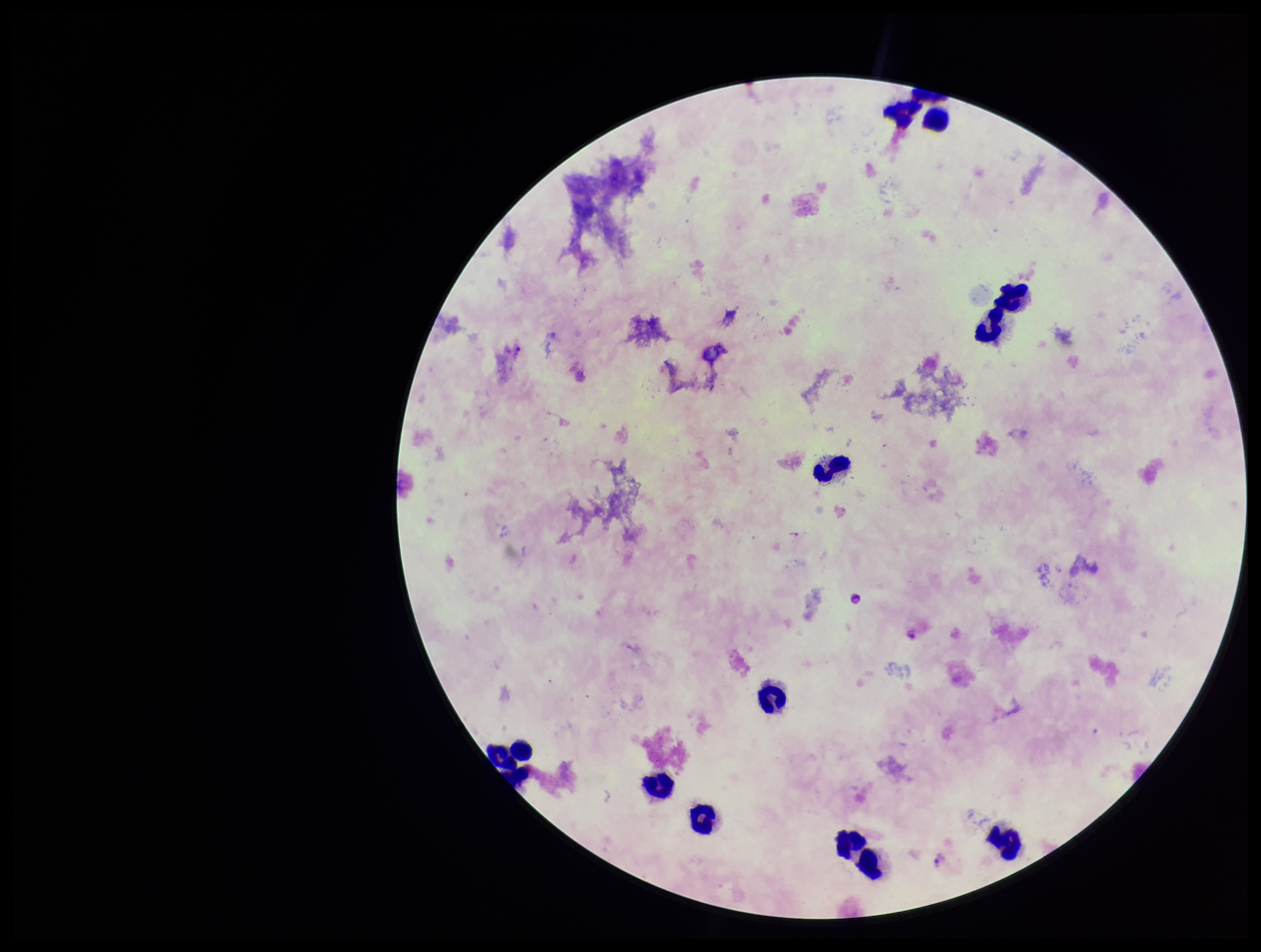
{
  "parasite_count": 3,
  "patient_malaria_status": "infected",
  "image_size": "1261×952 pixels",
  "field_of_view": "single",
  "stain": "Giemsa",
  "preparation": "thick blood smear",
  "capture": "smartphone photograph through the microscope eyepiece",
  "plasmodium_parasites": "seen",
  "leukocyte_count": 12,
  "species_reported_for_this_patient": "Plasmodium vivax"
}